Locate every malaria parasite and every leukocyte.
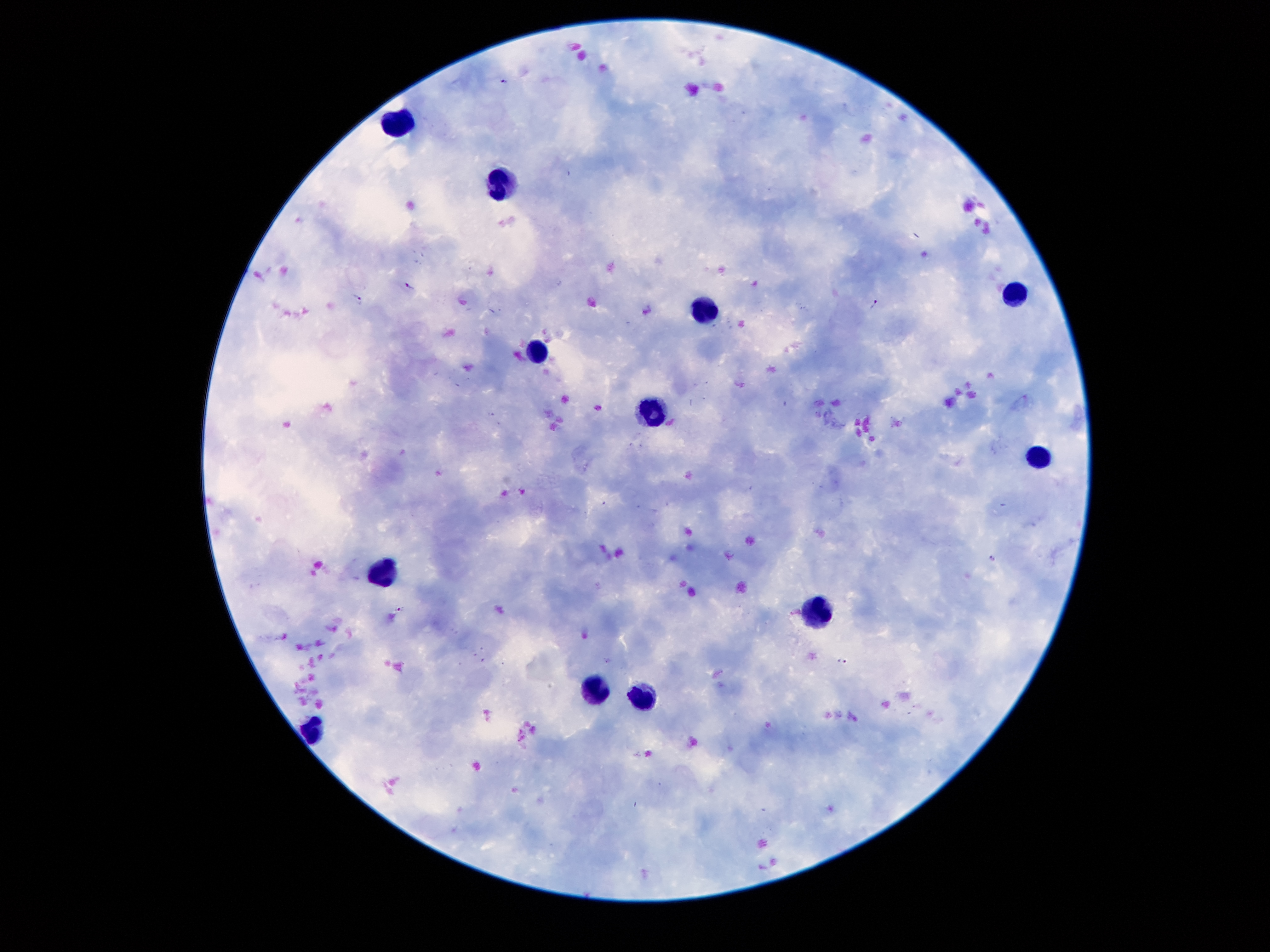
Approximate centers as [x, y] in pixels.
Malaria parasites: [503, 80], [410, 286], [358, 299], [875, 304], [993, 558], [401, 610], [841, 662].
Leukocytes: [403, 126], [503, 185], [1012, 295], [708, 311], [534, 350], [655, 414], [1041, 458], [382, 569], [817, 611], [595, 689], [643, 701], [311, 735].

Summary:
  - Magnification: 100x
  - Image size: 1270×952 pixels
  - Field of view: single
  - Capture: smartphone through the microscope eyepiece
  - Patient malaria status: positive for Plasmodium falciparum
  - Preparation: thick blood smear
  - Stain: Giemsa